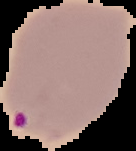

Malaria status: parasitized. From a thin blood smear. The area outside the segmented cell region is set to black. Image is 136×151 pixels.